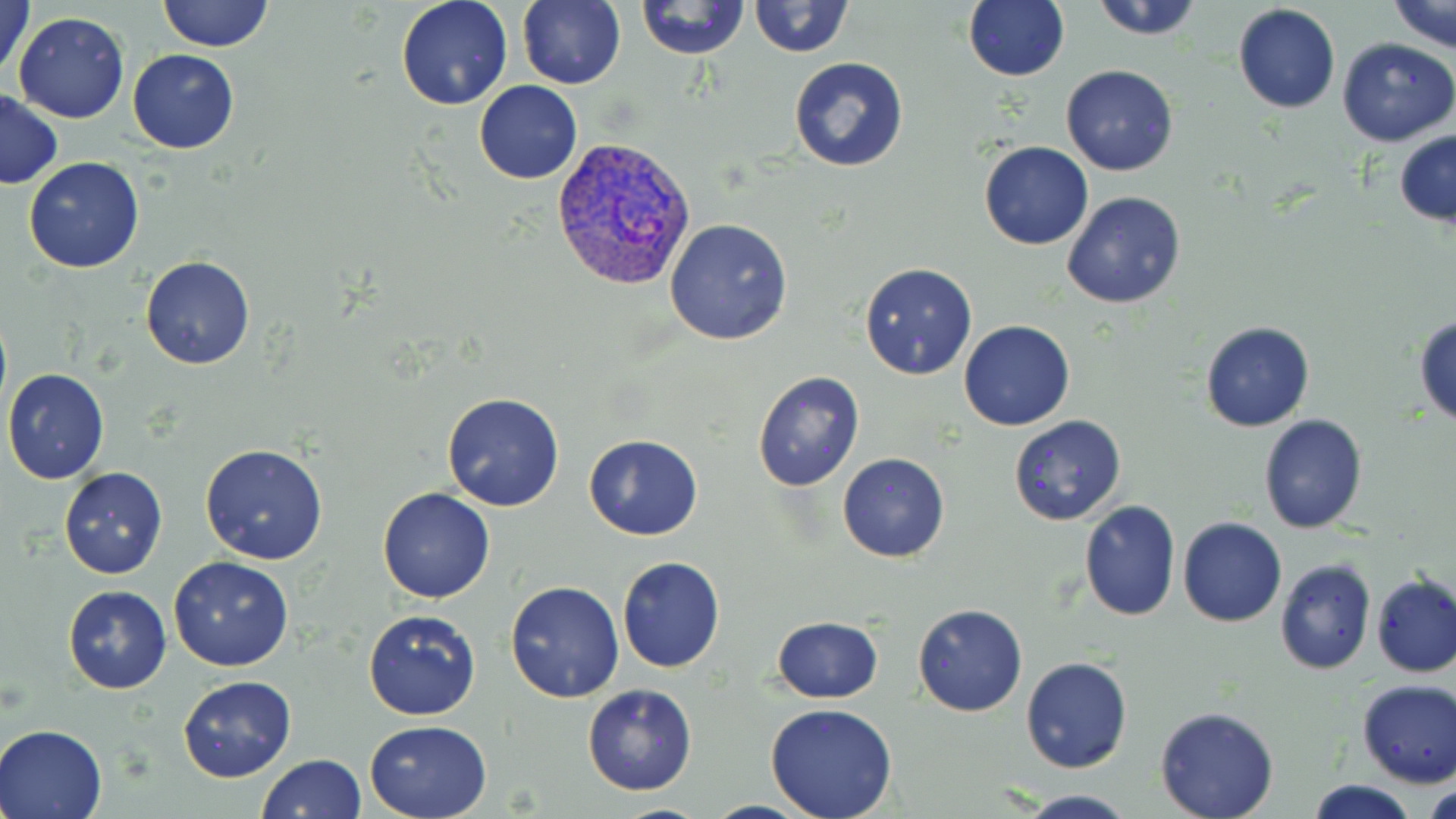
Summary:
  - Coordinate format: approximate bounding boxes as (x1, y1, x2, y2) in pixels
  - Uninfected red blood cell locations: (1, 0, 36, 84), (159, 0, 273, 51), (395, 0, 513, 110), (518, 0, 627, 90), (637, 0, 750, 59), (749, 0, 853, 58), (963, 0, 1068, 83), (1089, 0, 1205, 40), (1389, 0, 1454, 53), (1232, 5, 1341, 114), (12, 11, 130, 123), (1336, 37, 1455, 147), (127, 48, 238, 154), (789, 56, 908, 171), (1061, 65, 1178, 177), (474, 80, 583, 185), (2, 90, 63, 190), (1394, 130, 1456, 227), (979, 141, 1093, 251), (23, 157, 145, 272), (1062, 191, 1187, 310), (664, 218, 794, 345), (140, 256, 255, 370), (860, 263, 978, 380), (1414, 313, 1456, 427), (958, 320, 1075, 432), (1200, 321, 1315, 433), (2, 367, 110, 485), (753, 373, 865, 492), (441, 393, 564, 511), (1259, 414, 1369, 534), (1008, 415, 1127, 526), (584, 432, 704, 540), (199, 444, 329, 565), (838, 453, 950, 563), (58, 466, 168, 580), (377, 487, 495, 604), (1080, 499, 1181, 620), (1178, 516, 1287, 628), (169, 557, 295, 672), (616, 557, 725, 673), (1273, 559, 1375, 674), (1371, 574, 1456, 678), (504, 579, 626, 704), (62, 584, 171, 693), (913, 604, 1027, 717), (362, 608, 482, 720), (772, 617, 882, 702), (1021, 656, 1133, 775), (177, 675, 297, 784), (1356, 679, 1456, 787), (582, 683, 697, 795), (764, 702, 898, 819), (1155, 707, 1279, 819), (364, 719, 493, 817), (1, 724, 107, 818), (256, 753, 366, 819), (1305, 779, 1421, 818), (1422, 779, 1455, 816), (1016, 791, 1138, 818)
  - Plasmodium vivax-infected red blood cell locations: (551, 137, 699, 292)
  - Slide-level diagnosis: Plasmodium vivax
  - Magnification: 1000x
  - Field of view: one of a larger specimen
  - Image size: 1456×819 pixels
  - Stain: May-Grünwald-Giemsa
  - Preparation: thin blood film
  - Modality: light microscopy